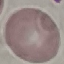

Result: no malaria parasites detected. Cell patch, automatically extracted from a larger field of view and resized to 64 × 64 pixels. Acquired by smartphone through the microscope eyepiece. Thin smear of blood. Giemsa stain.